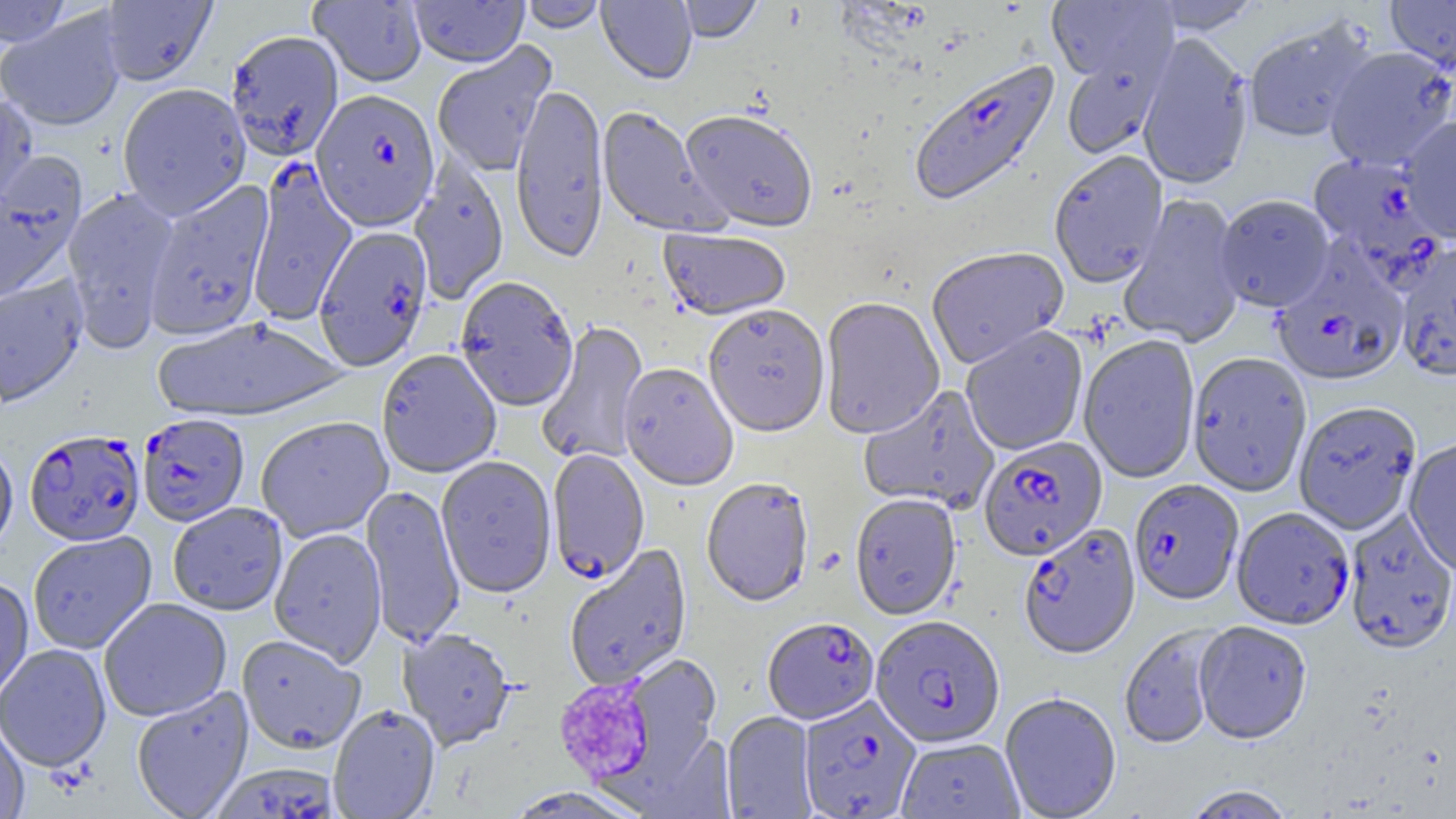
Summary:
  - Coordinate format: approximate bounding boxes as (x1, y1, x2, y2) in pixels
  - Uninfected red blood cell locations: (0, 0, 74, 47), (98, 0, 218, 86), (408, 0, 529, 69), (519, 0, 607, 34), (596, 0, 697, 86), (677, 0, 763, 45), (1150, 0, 1262, 35), (1385, 0, 1456, 74), (309, 1, 427, 88), (1046, 1, 1177, 87), (103, 2, 224, 177), (0, 9, 126, 132), (1244, 17, 1376, 143), (226, 30, 344, 163), (1137, 34, 1254, 192), (431, 41, 558, 177), (1324, 47, 1456, 171), (1061, 51, 1170, 160), (117, 83, 252, 220), (509, 83, 609, 264), (0, 92, 39, 218), (595, 107, 727, 239), (679, 112, 818, 234), (1398, 116, 1456, 243), (1049, 152, 1168, 289), (0, 156, 87, 305), (409, 160, 509, 306), (143, 179, 276, 341), (62, 187, 181, 352), (1119, 194, 1247, 349), (1214, 196, 1336, 314), (658, 229, 791, 322), (1394, 242, 1456, 384), (927, 248, 1069, 370), (0, 275, 88, 408), (455, 279, 578, 415), (820, 299, 944, 440), (703, 306, 830, 440), (151, 317, 348, 424), (536, 321, 649, 467), (960, 327, 1089, 457), (1078, 335, 1200, 484), (377, 351, 502, 480), (1187, 353, 1312, 497), (618, 364, 738, 493), (859, 385, 1000, 514), (1293, 402, 1422, 536), (255, 417, 394, 543), (1404, 439, 1456, 577), (0, 441, 18, 556), (435, 457, 557, 600), (701, 479, 814, 608), (360, 486, 464, 649), (850, 495, 961, 622), (168, 503, 288, 616), (1344, 509, 1456, 656), (269, 529, 387, 668), (27, 532, 157, 654), (564, 544, 693, 691), (0, 578, 34, 703), (99, 598, 232, 723), (1193, 622, 1312, 745), (1119, 626, 1224, 749), (398, 629, 515, 752), (236, 636, 366, 756), (0, 643, 112, 773), (616, 654, 723, 786), (131, 686, 254, 819), (999, 694, 1122, 819), (328, 706, 441, 819), (721, 712, 818, 819), (0, 718, 30, 818), (896, 738, 1025, 819), (1183, 785, 1295, 818), (504, 787, 643, 818)
  - Plasmodium falciparum-infected red blood cell locations: (909, 61, 1062, 209), (307, 86, 437, 229), (1308, 153, 1446, 283), (246, 161, 358, 325), (314, 227, 433, 372), (1273, 248, 1409, 388), (137, 414, 250, 527), (24, 430, 145, 546), (979, 438, 1108, 562), (547, 450, 650, 585), (1129, 480, 1243, 607), (1231, 509, 1354, 631), (1019, 525, 1141, 661), (870, 617, 1006, 749), (763, 619, 879, 725), (799, 696, 921, 819), (210, 763, 339, 819)
  - Platelet locations: (554, 678, 655, 784)
  - Slide-level diagnosis: Plasmodium falciparum
  - Image size: 1456×819 pixels
  - Modality: optical microscopy
  - Preparation: thin blood film
  - Magnification: 1000x
  - Field of view: one of a larger specimen